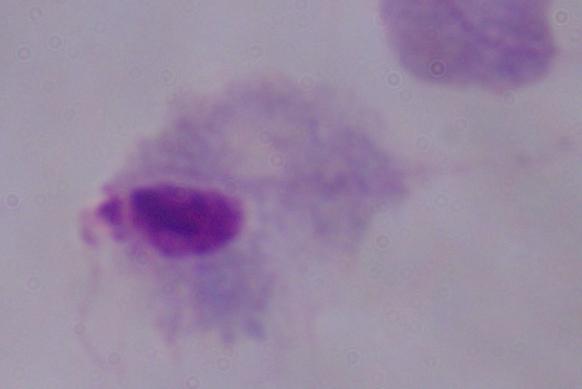

A trichomonad is shown. Micrograph. 1000x magnification.